Classify this cell by malaria status.
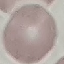

Uninfected.

Thin blood film. Automatically extracted cell patch, resized to 64 × 64 pixels. Acquired by smartphone through the microscope eyepiece. Giemsa stain.